Identify the parasite.
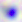
Toxoplasma gondii.

Summary:
  - Magnification: 400x
  - Modality: micrograph